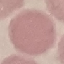

malaria status = uninfected
preparation = thin blood film
stain = Giemsa
capture = smartphone camera at the microscope eyepiece
image type = cell patch, automatically extracted from a larger field of view and resized to 64 × 64 pixels